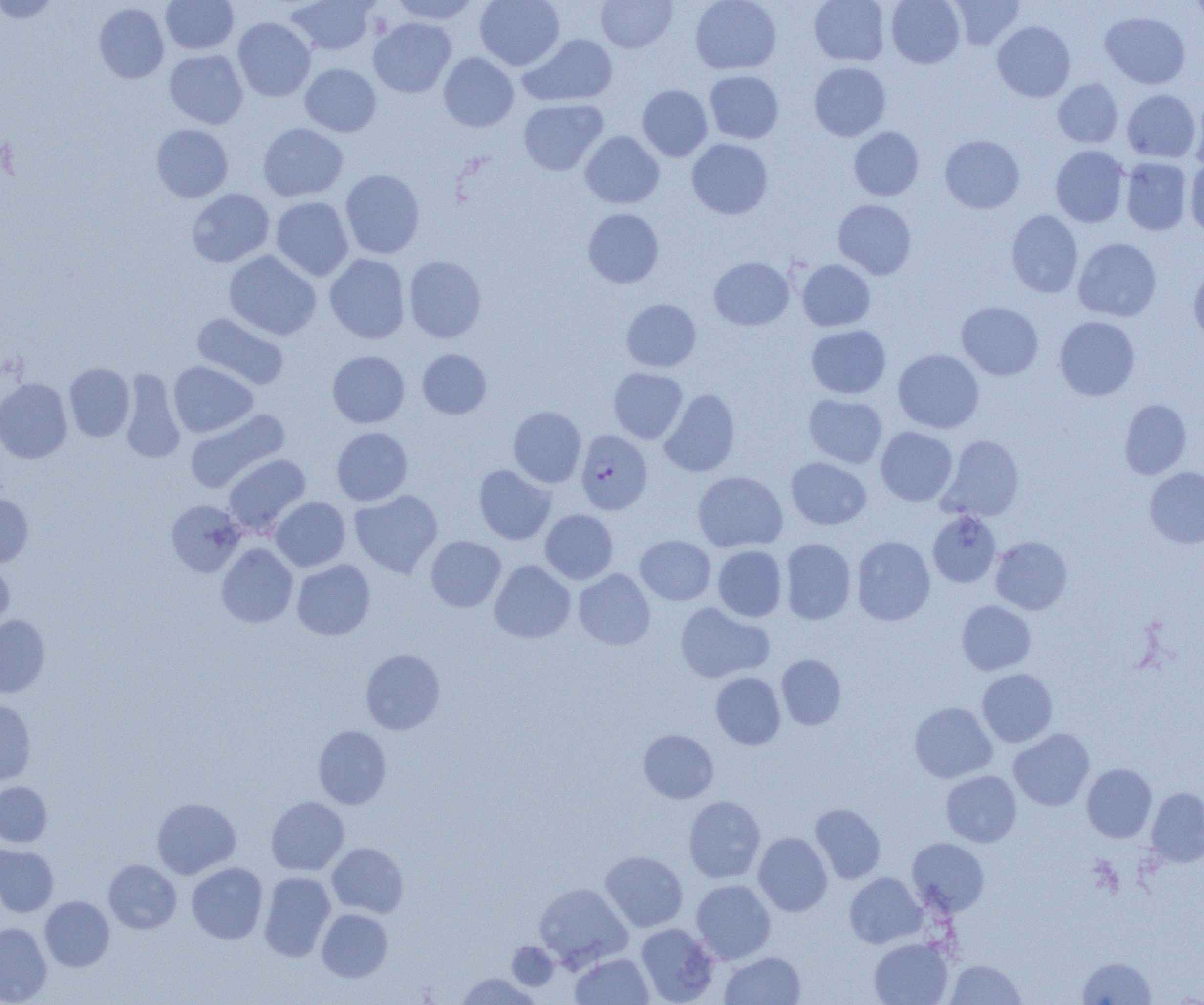
Summary:
  - Coordinate format: approximate bounding boxes as named x1/y1/x2/y2 corners in pixels
  - Uninfected red blood cell locations: (x1=0, y1=0, x2=60, y2=22), (x1=160, y1=0, x2=239, y2=54), (x1=287, y1=0, x2=377, y2=55), (x1=390, y1=0, x2=481, y2=24), (x1=475, y1=0, x2=564, y2=70), (x1=596, y1=0, x2=678, y2=53), (x1=690, y1=0, x2=781, y2=74), (x1=809, y1=0, x2=890, y2=66), (x1=886, y1=0, x2=965, y2=68), (x1=949, y1=0, x2=1025, y2=50), (x1=1190, y1=0, x2=1204, y2=29), (x1=93, y1=3, x2=169, y2=83), (x1=1100, y1=10, x2=1190, y2=89), (x1=1112, y1=11, x2=1195, y2=164), (x1=233, y1=17, x2=316, y2=101), (x1=368, y1=18, x2=456, y2=98), (x1=992, y1=21, x2=1075, y2=102), (x1=519, y1=33, x2=618, y2=107), (x1=164, y1=49, x2=248, y2=128), (x1=438, y1=52, x2=519, y2=132), (x1=809, y1=62, x2=891, y2=141), (x1=300, y1=63, x2=381, y2=137), (x1=705, y1=70, x2=784, y2=144), (x1=1053, y1=78, x2=1123, y2=148), (x1=637, y1=85, x2=712, y2=161), (x1=1122, y1=89, x2=1201, y2=163), (x1=1189, y1=92, x2=1204, y2=170), (x1=518, y1=98, x2=608, y2=175), (x1=258, y1=123, x2=348, y2=202), (x1=150, y1=124, x2=233, y2=202), (x1=848, y1=127, x2=924, y2=200), (x1=580, y1=131, x2=664, y2=208), (x1=940, y1=135, x2=1025, y2=213), (x1=687, y1=138, x2=773, y2=219), (x1=1051, y1=145, x2=1129, y2=227), (x1=1120, y1=157, x2=1193, y2=235), (x1=1185, y1=157, x2=1204, y2=237), (x1=340, y1=169, x2=425, y2=259), (x1=186, y1=188, x2=274, y2=267), (x1=270, y1=196, x2=353, y2=281), (x1=833, y1=199, x2=917, y2=280), (x1=583, y1=208, x2=664, y2=288), (x1=1006, y1=210, x2=1083, y2=297), (x1=1073, y1=238, x2=1162, y2=322), (x1=223, y1=250, x2=321, y2=340), (x1=325, y1=254, x2=410, y2=344), (x1=404, y1=256, x2=486, y2=342), (x1=709, y1=257, x2=793, y2=330), (x1=796, y1=259, x2=875, y2=331), (x1=1188, y1=262, x2=1204, y2=346), (x1=621, y1=299, x2=701, y2=371), (x1=956, y1=301, x2=1043, y2=381), (x1=191, y1=313, x2=289, y2=390), (x1=1055, y1=316, x2=1139, y2=400), (x1=806, y1=325, x2=891, y2=398), (x1=417, y1=349, x2=492, y2=419), (x1=893, y1=349, x2=984, y2=433), (x1=327, y1=351, x2=409, y2=428), (x1=168, y1=361, x2=257, y2=437), (x1=64, y1=363, x2=134, y2=442), (x1=608, y1=367, x2=687, y2=443), (x1=119, y1=370, x2=185, y2=463), (x1=0, y1=378, x2=72, y2=463), (x1=659, y1=389, x2=740, y2=477), (x1=804, y1=393, x2=888, y2=468), (x1=1119, y1=398, x2=1192, y2=479), (x1=508, y1=406, x2=586, y2=488), (x1=185, y1=408, x2=289, y2=493), (x1=875, y1=426, x2=957, y2=506), (x1=331, y1=427, x2=413, y2=506), (x1=939, y1=434, x2=1024, y2=521), (x1=223, y1=453, x2=311, y2=537), (x1=786, y1=457, x2=872, y2=530), (x1=474, y1=464, x2=556, y2=545), (x1=1144, y1=466, x2=1204, y2=548), (x1=693, y1=471, x2=788, y2=553), (x1=349, y1=489, x2=442, y2=578), (x1=0, y1=492, x2=33, y2=567), (x1=269, y1=496, x2=350, y2=571), (x1=166, y1=500, x2=246, y2=577), (x1=540, y1=509, x2=618, y2=584), (x1=928, y1=510, x2=1001, y2=587), (x1=425, y1=535, x2=506, y2=612), (x1=635, y1=535, x2=716, y2=605), (x1=852, y1=536, x2=935, y2=625), (x1=990, y1=536, x2=1072, y2=614), (x1=780, y1=538, x2=856, y2=624), (x1=216, y1=543, x2=298, y2=628), (x1=713, y1=545, x2=787, y2=622), (x1=291, y1=559, x2=375, y2=640), (x1=489, y1=559, x2=575, y2=643), (x1=0, y1=560, x2=14, y2=634), (x1=574, y1=569, x2=655, y2=650), (x1=956, y1=600, x2=1036, y2=675), (x1=675, y1=601, x2=774, y2=683), (x1=0, y1=615, x2=50, y2=697), (x1=360, y1=648, x2=445, y2=734), (x1=776, y1=654, x2=846, y2=730), (x1=976, y1=668, x2=1057, y2=747), (x1=710, y1=672, x2=786, y2=750), (x1=0, y1=700, x2=36, y2=784), (x1=909, y1=702, x2=997, y2=783), (x1=313, y1=725, x2=391, y2=808), (x1=1009, y1=728, x2=1095, y2=810), (x1=638, y1=729, x2=718, y2=803), (x1=1082, y1=763, x2=1157, y2=842), (x1=941, y1=770, x2=1022, y2=847), (x1=0, y1=781, x2=52, y2=847), (x1=1146, y1=787, x2=1204, y2=867), (x1=683, y1=795, x2=765, y2=883), (x1=266, y1=796, x2=349, y2=875), (x1=152, y1=797, x2=241, y2=879), (x1=810, y1=804, x2=886, y2=883), (x1=753, y1=832, x2=832, y2=916), (x1=908, y1=838, x2=989, y2=915), (x1=327, y1=843, x2=408, y2=918), (x1=0, y1=844, x2=58, y2=917), (x1=600, y1=850, x2=688, y2=932), (x1=103, y1=859, x2=181, y2=934), (x1=187, y1=862, x2=267, y2=944), (x1=259, y1=871, x2=335, y2=961), (x1=845, y1=873, x2=926, y2=948), (x1=691, y1=879, x2=776, y2=963), (x1=534, y1=882, x2=633, y2=970), (x1=40, y1=896, x2=114, y2=971), (x1=317, y1=908, x2=393, y2=981), (x1=0, y1=922, x2=51, y2=1004), (x1=636, y1=923, x2=719, y2=1004), (x1=869, y1=938, x2=953, y2=1005), (x1=507, y1=941, x2=559, y2=990), (x1=720, y1=951, x2=805, y2=1005), (x1=570, y1=952, x2=654, y2=1004), (x1=1077, y1=956, x2=1157, y2=1004), (x1=944, y1=959, x2=1026, y2=1004), (x1=456, y1=973, x2=539, y2=1005)
  - Plasmodium falciparum-infected red blood cell locations: (x1=576, y1=429, x2=652, y2=514)
  - Slide-level diagnosis: Plasmodium falciparum
  - Preparation: thin blood film
  - Modality: optical microscopy
  - Field of view: one of a larger specimen
  - Magnification: 1000x
  - Image size: 1204×1005 pixels